Assess this cell for malaria.
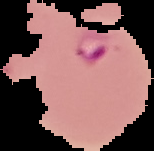
Parasitized.

Summary:
  - Image type: segmented cell region with the area outside set to black
  - Preparation: thin blood film
  - Image size: 154×151 pixels